Locate and identify every blood parasite.
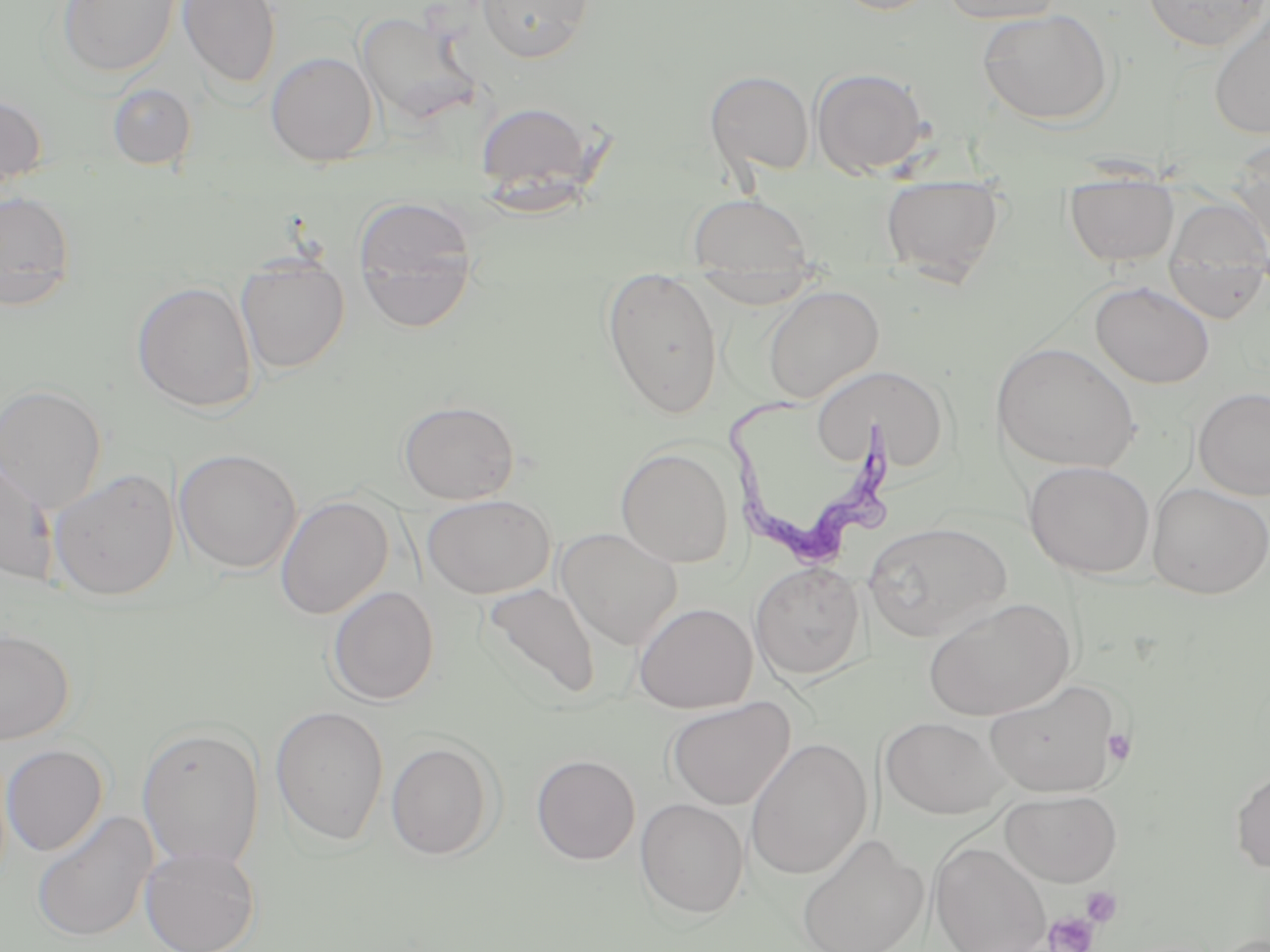
Approximate bounding boxes as named x1/y1/x2/y2 corners in pixels.
Trypanosoma brucei: (x1=724, y1=397, x2=901, y2=572).
No Plasmodium falciparum, Plasmodium ovale, Plasmodium malariae, Plasmodium vivax, or Babesia divergens observed.

Uninfected red blood cell locations: (x1=55, y1=0, x2=180, y2=79), (x1=177, y1=0, x2=281, y2=89), (x1=476, y1=0, x2=594, y2=63), (x1=829, y1=0, x2=941, y2=16), (x1=939, y1=0, x2=1068, y2=25), (x1=1143, y1=0, x2=1268, y2=53), (x1=976, y1=8, x2=1115, y2=126), (x1=1208, y1=9, x2=1270, y2=141), (x1=355, y1=11, x2=482, y2=129), (x1=266, y1=51, x2=378, y2=166), (x1=811, y1=67, x2=930, y2=177), (x1=705, y1=70, x2=814, y2=178), (x1=107, y1=82, x2=196, y2=170), (x1=0, y1=92, x2=48, y2=193), (x1=474, y1=101, x2=596, y2=201), (x1=1229, y1=140, x2=1270, y2=254), (x1=880, y1=177, x2=1007, y2=283), (x1=1064, y1=180, x2=1179, y2=266), (x1=0, y1=190, x2=76, y2=309), (x1=686, y1=194, x2=815, y2=271), (x1=354, y1=196, x2=478, y2=329), (x1=1163, y1=201, x2=1270, y2=323), (x1=236, y1=256, x2=350, y2=373), (x1=602, y1=271, x2=724, y2=419), (x1=689, y1=272, x2=824, y2=306), (x1=132, y1=281, x2=259, y2=413), (x1=1091, y1=281, x2=1214, y2=388), (x1=762, y1=285, x2=884, y2=403), (x1=992, y1=341, x2=1142, y2=474), (x1=812, y1=364, x2=952, y2=475), (x1=0, y1=383, x2=107, y2=514), (x1=1193, y1=387, x2=1270, y2=499), (x1=399, y1=400, x2=520, y2=504), (x1=616, y1=446, x2=734, y2=567), (x1=174, y1=448, x2=302, y2=575), (x1=0, y1=455, x2=59, y2=586), (x1=1024, y1=460, x2=1156, y2=578), (x1=49, y1=468, x2=179, y2=602), (x1=1147, y1=482, x2=1269, y2=598), (x1=421, y1=494, x2=556, y2=599), (x1=275, y1=495, x2=393, y2=620), (x1=863, y1=521, x2=1013, y2=641), (x1=555, y1=528, x2=683, y2=650), (x1=750, y1=562, x2=866, y2=680), (x1=480, y1=582, x2=601, y2=703), (x1=328, y1=586, x2=439, y2=706), (x1=923, y1=597, x2=1076, y2=721), (x1=633, y1=602, x2=757, y2=713), (x1=0, y1=629, x2=75, y2=745), (x1=983, y1=679, x2=1124, y2=797), (x1=666, y1=696, x2=796, y2=810), (x1=270, y1=704, x2=390, y2=846), (x1=880, y1=716, x2=1012, y2=819), (x1=136, y1=725, x2=265, y2=871), (x1=746, y1=737, x2=872, y2=880), (x1=386, y1=741, x2=497, y2=860), (x1=1, y1=744, x2=108, y2=857), (x1=531, y1=754, x2=640, y2=865), (x1=1230, y1=764, x2=1270, y2=874), (x1=999, y1=789, x2=1123, y2=887), (x1=635, y1=798, x2=750, y2=919), (x1=31, y1=810, x2=158, y2=942), (x1=796, y1=832, x2=929, y2=952), (x1=930, y1=841, x2=1052, y2=952), (x1=139, y1=844, x2=260, y2=952). Platelet locations: (x1=1102, y1=728, x2=1136, y2=764), (x1=1081, y1=886, x2=1123, y2=927), (x1=1044, y1=912, x2=1098, y2=952). Slide-level diagnosis: Trypanosoma brucei. One field of a larger specimen. Captured at 1000x magnification. Image is 1270×952 pixels. Thin blood film. May-Grünwald-Giemsa stain. Optical microscopy.